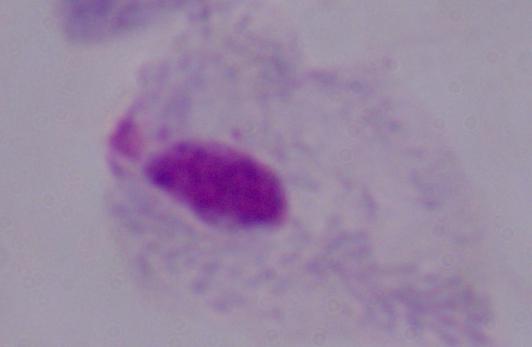
magnification: 1000x
modality: micrograph
identification: trichomonad